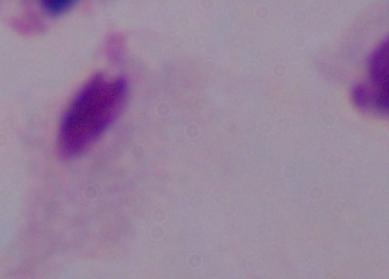
{
  "magnification": "1000x",
  "identification": "trichomonad",
  "modality": "photomicrograph"
}